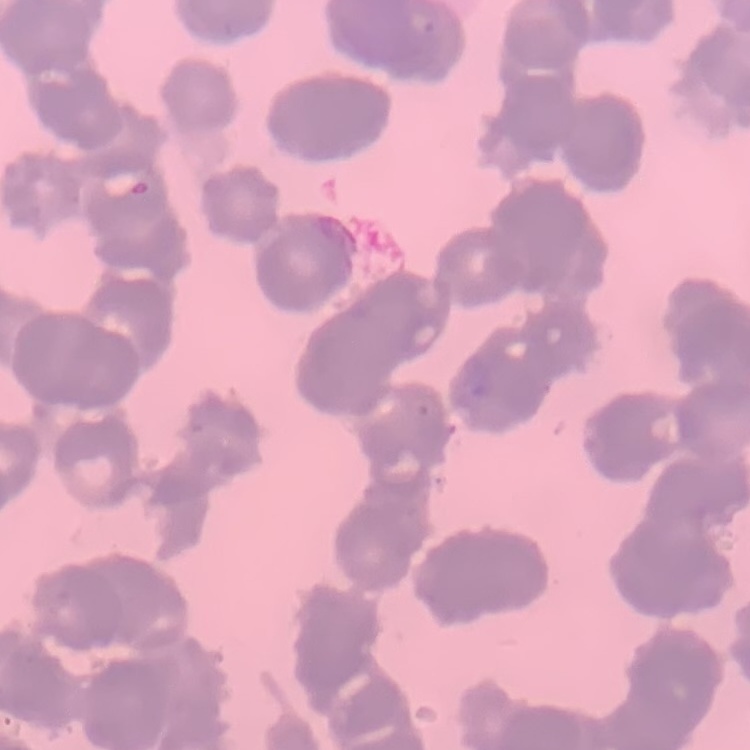

The erythrocytes exhibit rouleaux formation. Thin blood film. Field's or Giemsa stain. One tile cut from a larger photomicrograph.